Assess the morphology of the erythrocytes.
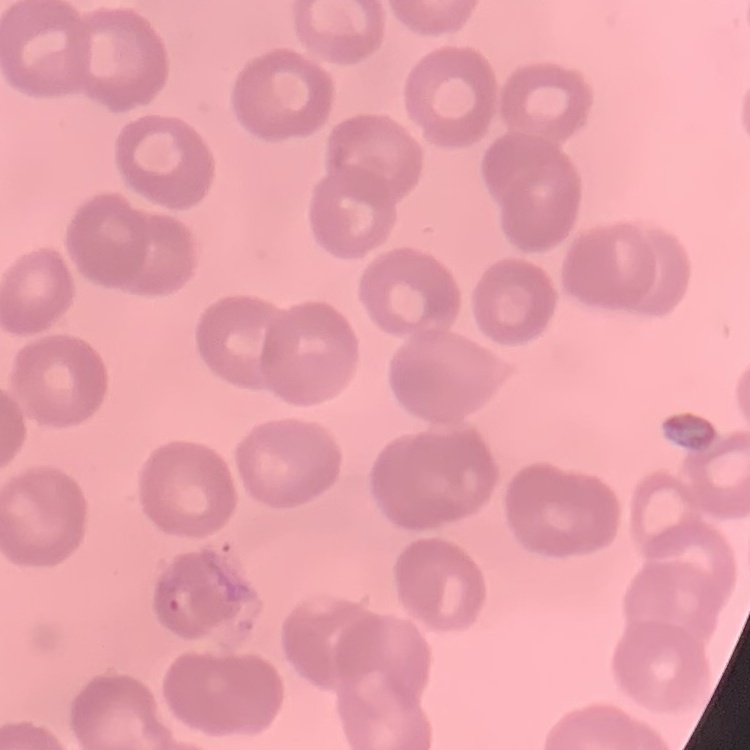
They show no rouleaux formation.

Summary:
  - Stain: Field's or Giemsa
  - Preparation: thin blood film
  - Image type: one tile cut from a larger photomicrograph